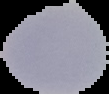
Summary:
  - Malaria status: uninfected
  - Preparation: thin blood smear
  - Image size: 109×94 pixels
  - Image type: segmented cell region with the area outside set to black